Assess this cell for malaria.
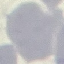

It is uninfected.

Summary:
  - Preparation: thin blood smear
  - Capture: smartphone camera at the microscope eyepiece
  - Stain: Giemsa
  - Image type: automatically extracted cell patch, resized to 64 × 64 pixels